Comment on the morphology of the red blood cells.
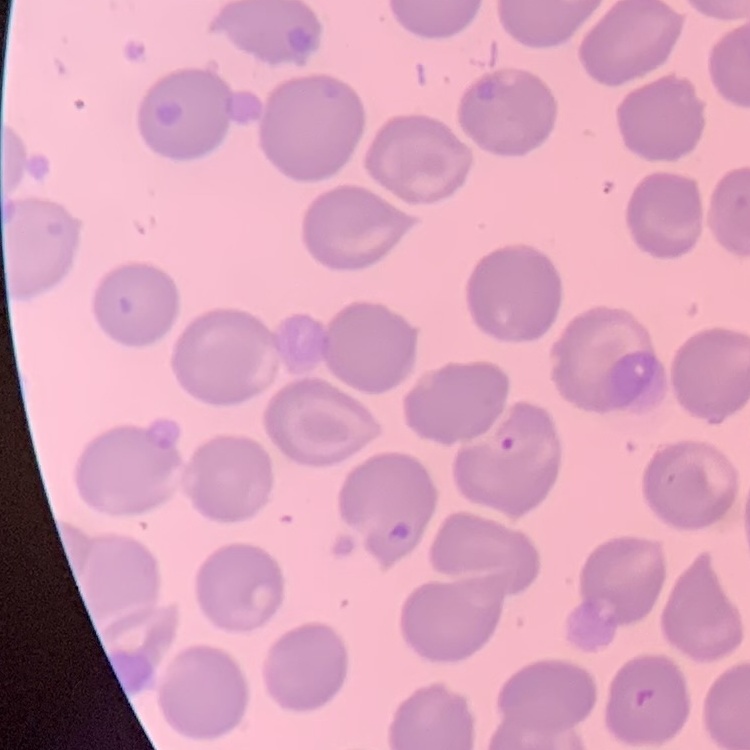
No rouleaux formation.

Square crop of a larger photomicrograph. Field's or Giemsa stain. Thin blood film.